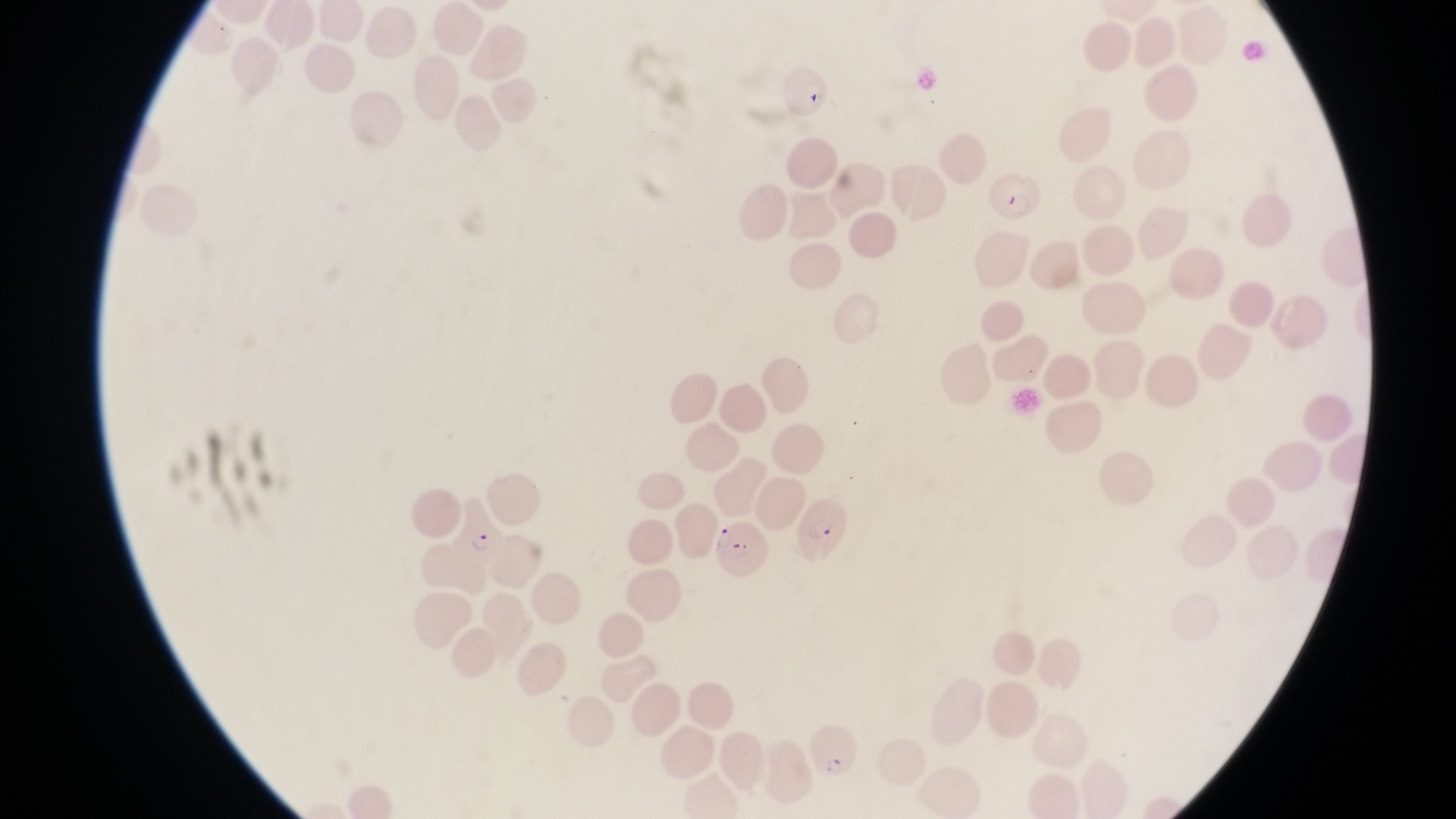

Approximate bounding boxes as [left, top, right, bottom] in pixels.
Summary:
  - Parasitised red blood cell locations: [984, 169, 1044, 222], [795, 489, 859, 574], [452, 497, 510, 566], [716, 522, 774, 588], [802, 717, 863, 781]
  - Magnification: 1000x
  - Field of view: single
  - Image size: 1456×819 pixels
  - Capture: smartphone photograph through the eyepiece of an Olympus CX-23 microscope
  - Preparation: thin blood film
  - Country: Uganda